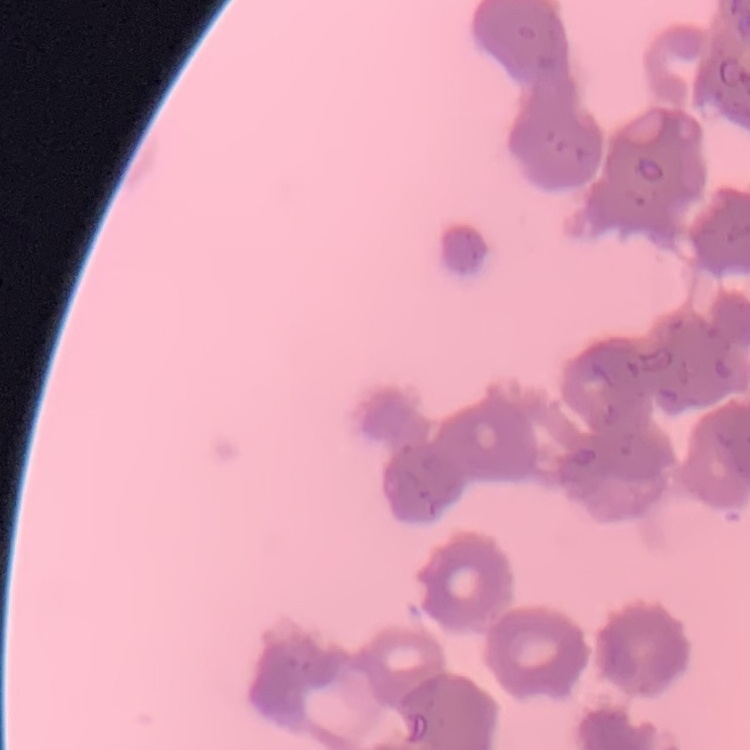

The red blood cells show rouleaux formation. Stained with either Field's or Giemsa. One tile cut from a larger photomicrograph. Thin peripheral smear.